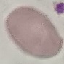
Result: negative for malaria parasites. Thin blood film. Acquired by smartphone through the microscope eyepiece. Automatically extracted cell patch, resized to 64 × 64 pixels. Giemsa stain.